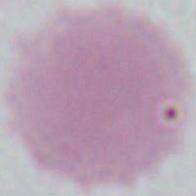
A red blood cell is seen. Captured at 1000x magnification. Photomicrograph.